Comment on the morphology of the erythrocytes.
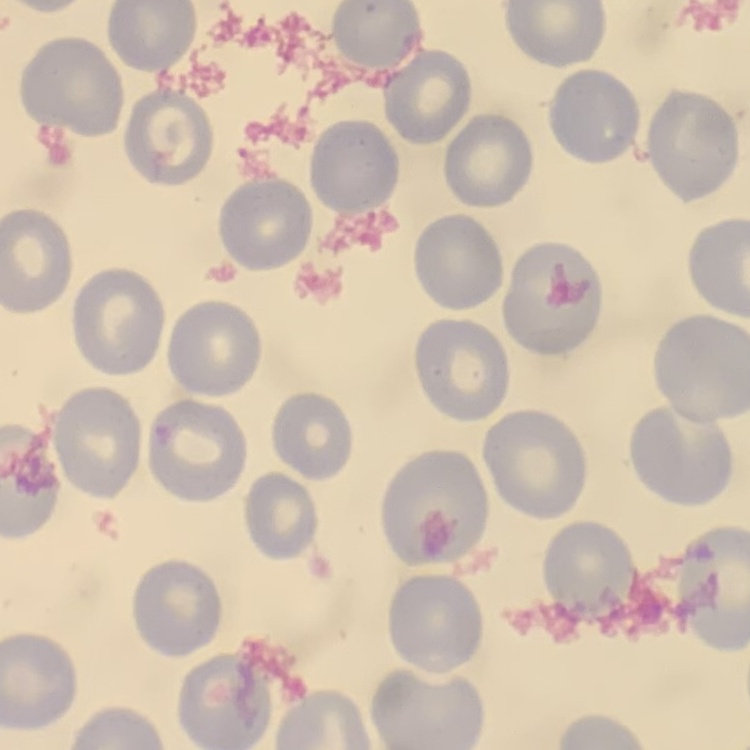

They show no rouleaux formation.

Stained with either Field's or Giemsa. Thin blood smear. Square crop of a larger photomicrograph.